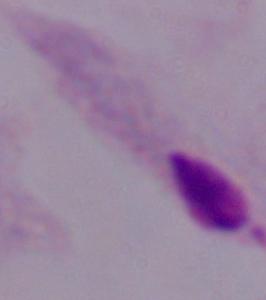
Photomicrograph. A trichomonad is seen. Captured at 1000x magnification.